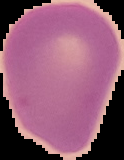

image size = 124×160 pixels
malaria status = uninfected
preparation = thin blood smear
image type = segmented cell region with the area outside set to black